Report the malaria status of this cell.
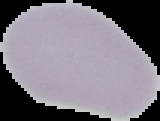
Uninfected.

{
  "image_type": "cell region segmented out of the field of view; surrounding area masked to black",
  "image_size": "160×121 pixels",
  "preparation": "thin blood film"
}